Report the malaria status of this cell.
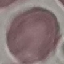

It is uninfected.

Thin blood film. Cell patch, automatically extracted from a larger field of view and resized to 64 × 64 pixels. Giemsa-stained preparation. Photographed with a smartphone camera at the microscope eyepiece.